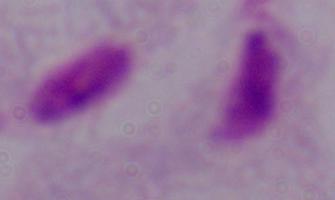
Summary:
  - Modality: photomicrograph
  - Magnification: 1000x
  - Identification: trichomonad